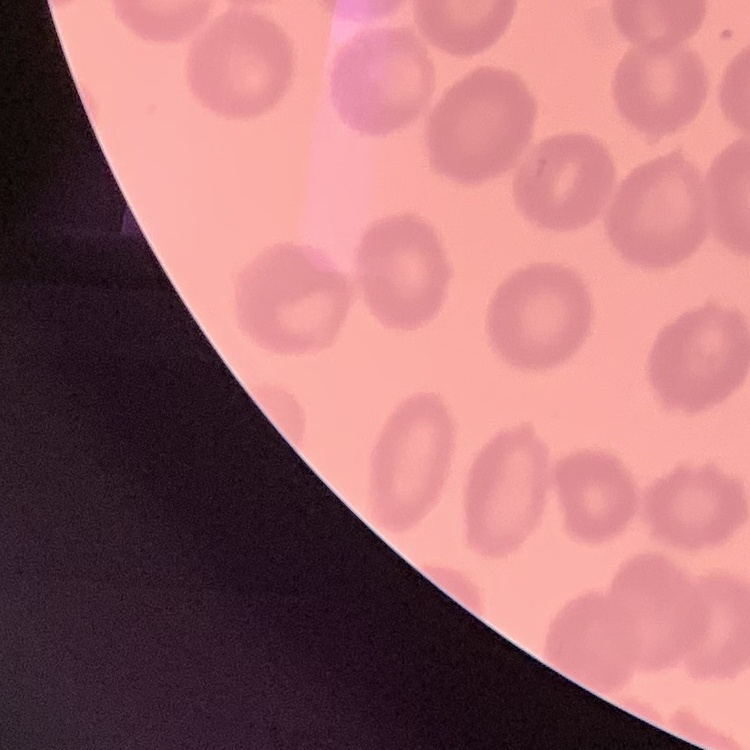

{
  "erythrocyte_morphology": "no rouleaux formation",
  "image_type": "one tile cut from a larger photomicrograph",
  "preparation": "thin blood film",
  "stain": "Field's or Giemsa"
}